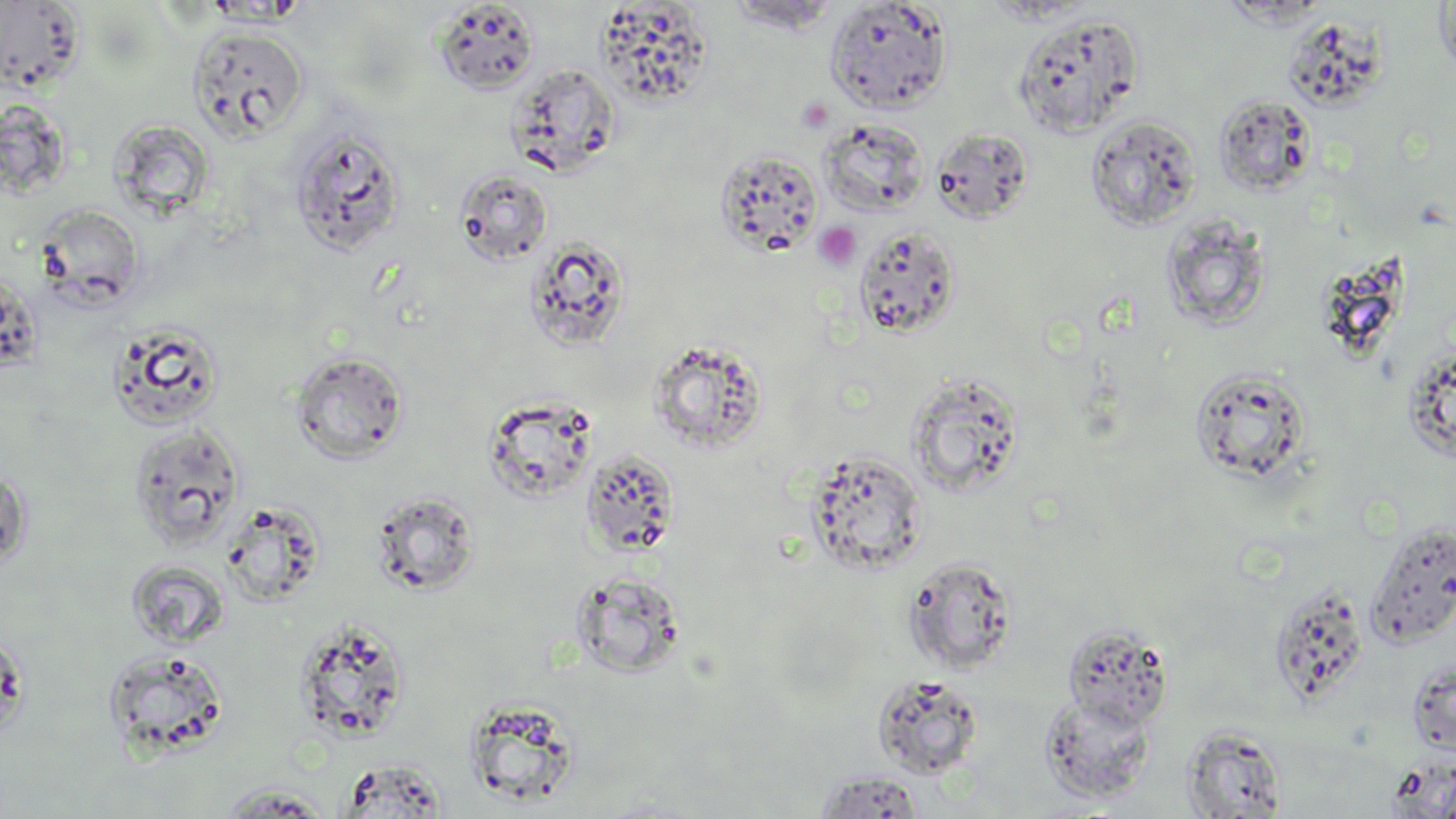
Summary:
  - Coordinate format: approximate bounding boxes as (x1,y1)-(x2,y2) corner pairs in pixels
  - Platelet locations: (796,97)-(835,133), (813,221)-(862,272)
  - Uninfected red blood cell locations: (724,0)-(843,33), (1434,0)-(1456,85), (0,1)-(86,94), (434,1)-(539,94), (823,1)-(953,113), (594,2)-(713,108), (1013,13)-(1145,138), (1283,17)-(1392,117), (187,25)-(309,142), (506,63)-(621,176), (1213,93)-(1317,198), (1086,115)-(1201,232), (110,117)-(214,217), (818,117)-(929,218), (290,126)-(407,256), (931,128)-(1034,224), (714,148)-(825,258), (454,169)-(552,266), (35,204)-(145,309), (1161,214)-(1271,332), (853,226)-(961,339), (524,237)-(631,352), (1315,249)-(1409,367), (107,321)-(226,431), (646,338)-(769,454), (1402,344)-(1456,465), (290,350)-(409,464), (1189,366)-(1311,485), (905,371)-(1026,498), (483,394)-(598,503), (128,423)-(246,550), (581,448)-(681,558), (804,448)-(928,575), (371,490)-(482,596), (1363,520)-(1456,649), (904,555)-(1018,674), (125,559)-(229,650), (570,570)-(688,678), (1267,584)-(1371,710), (293,618)-(411,744), (1061,623)-(1173,730), (0,628)-(28,742), (101,647)-(232,760), (1406,657)-(1456,755), (872,673)-(984,780), (1039,692)-(1157,804), (1181,726)-(1288,818), (338,759)-(448,817), (813,770)-(927,817), (1438,774)-(1456,819), (213,785)-(334,817)
  - Slide-level diagnosis: no evidence of blood parasites
  - Modality: optical microscopy
  - Stain: May-Grünwald-Giemsa
  - Field of view: single
  - Preparation: thin blood smear
  - Image size: 1456×819 pixels
  - Magnification: 1000x